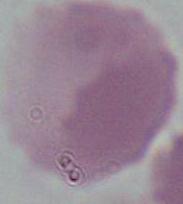

Summary:
  - Identification: red blood cell
  - Magnification: 1000x
  - Modality: micrograph